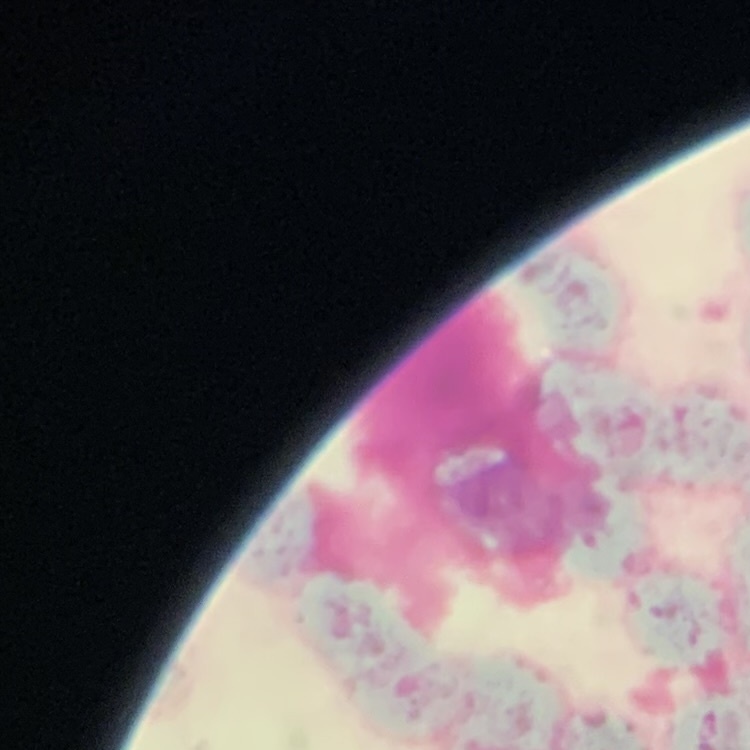

The red blood cells exhibit rouleaux formation. Field's or Giemsa stain. One tile cut from a larger photomicrograph. Thin blood film.